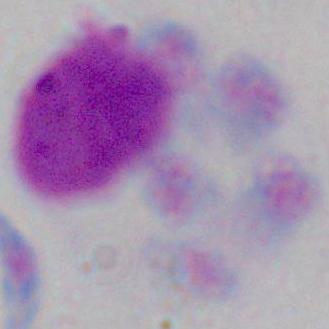

identification: leukocyte
magnification: 1000x
modality: micrograph